State which cell type is depicted.
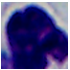
A leukocyte.

1000x magnification. Photomicrograph.